Report the malaria status of this cell.
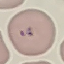
It is parasitized.

Cell patch, automatically extracted from a larger field of view and resized to 64 × 64 pixels. Giemsa-stained preparation. Photographed with a smartphone camera at the microscope eyepiece. Thin smear of blood.